Describe the morphology of the erythrocytes.
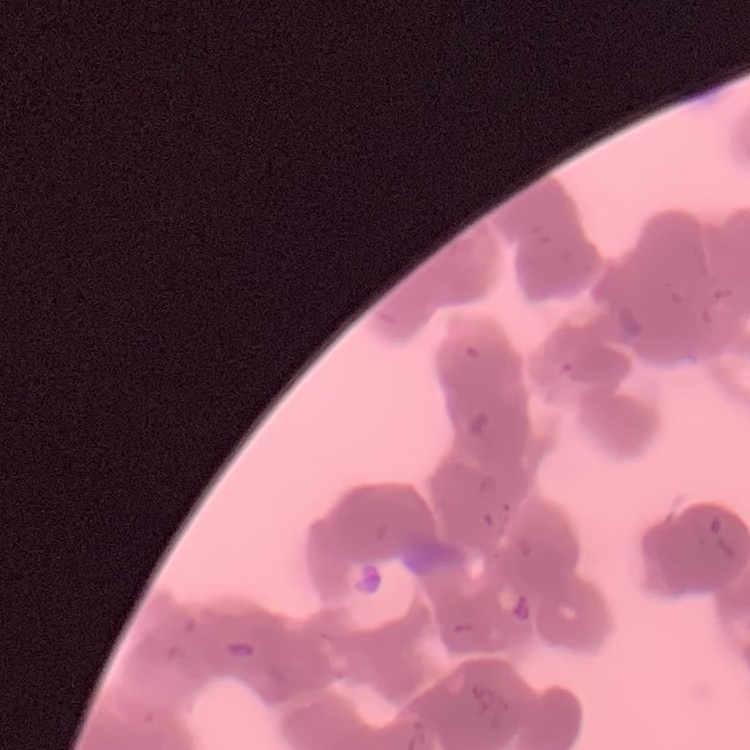
Rouleaux formation.

Thin peripheral smear. One tile cut from a larger photomicrograph. Field's or Giemsa stain.